Assess this cell for malaria.
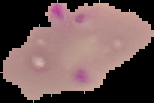

It is parasitized.

Summary:
  - Preparation: thin blood smear
  - Image size: 154×103 pixels
  - Image type: segmented cell region on a black background